Assess this cell for malaria.
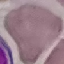

It is uninfected.

Cell patch, automatically extracted from a larger field of view and resized to 64 × 64 pixels. Photographed with a smartphone camera at the microscope eyepiece. Giemsa-stained preparation. Thin smear of blood.